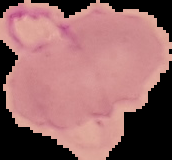
The area outside the segmented cell region is set to black. From a thin blood film. Image is 172×160 pixels. Malaria status: parasitized.